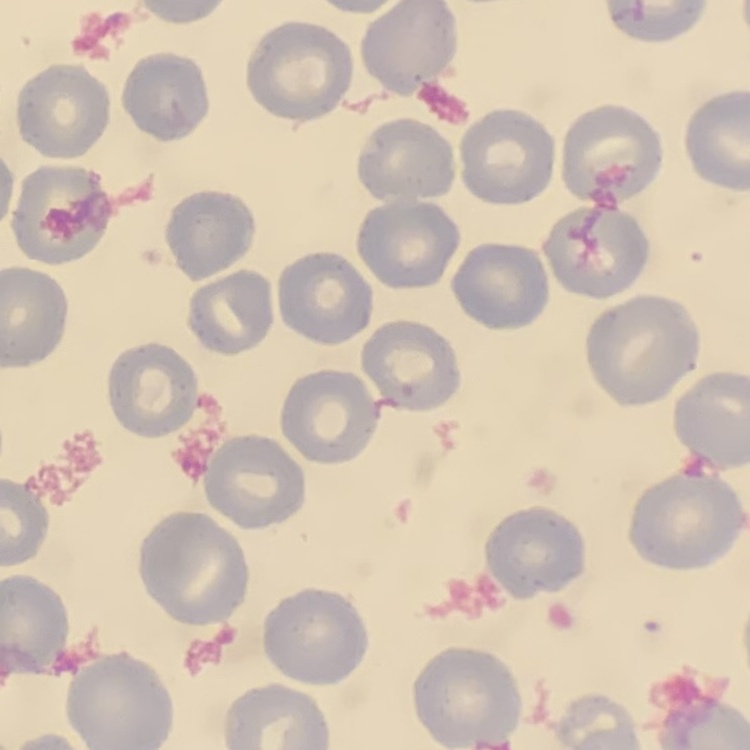

Summary:
  - Red blood cell morphology: no rouleaux formation
  - Preparation: thin blood film
  - Image type: square crop of a larger photomicrograph
  - Stain: Field's or Giemsa